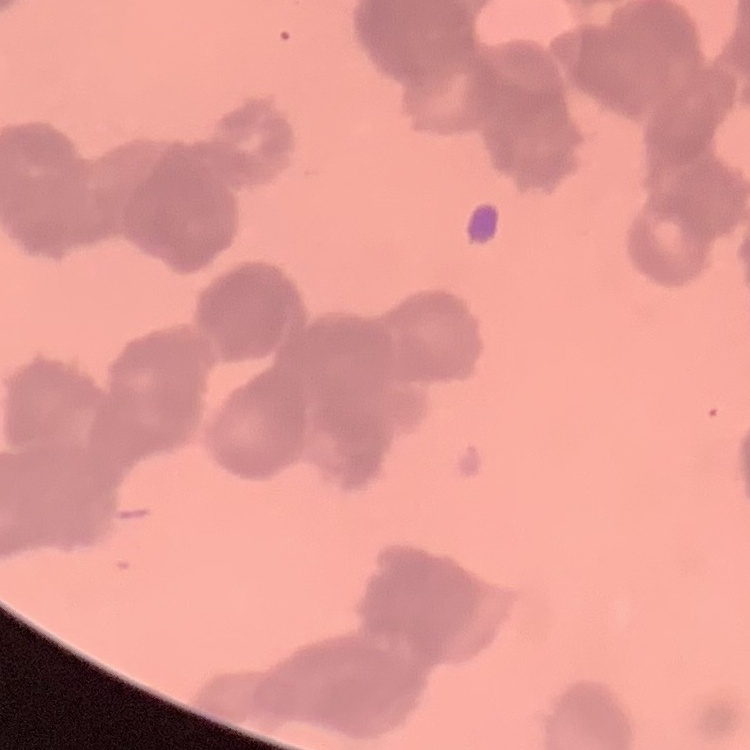

Summary:
  - Erythrocyte morphology: rouleaux formation
  - Image type: square crop of a larger photomicrograph
  - Stain: Field's or Giemsa
  - Preparation: thin blood film